Identify the blood parasite species.
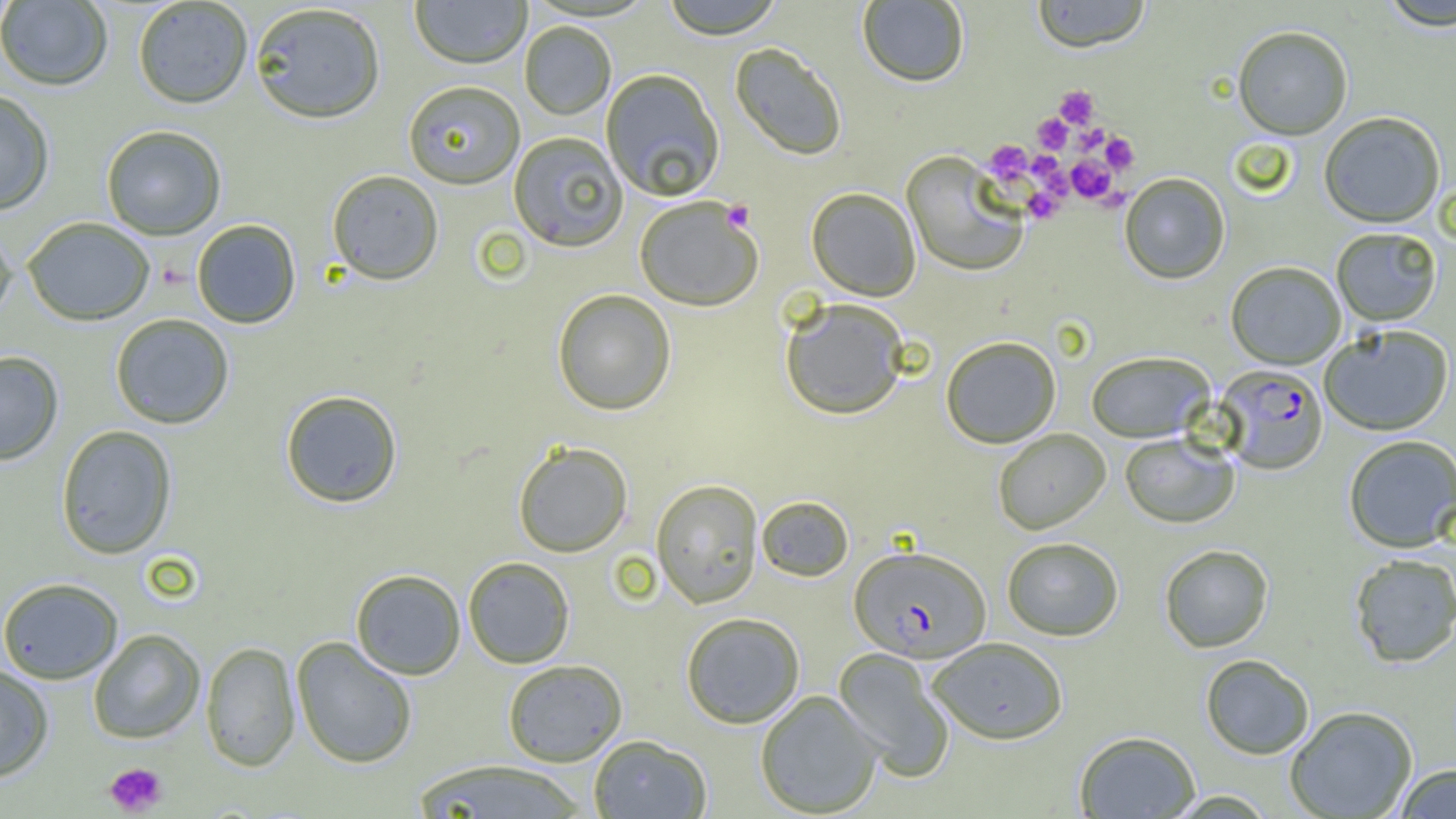

Plasmodium falciparum.

Approximate bounding boxes as named x1/y1/x2/y2 corners in pixels. Platelet locations: (x1=1054, y1=85, x2=1100, y2=128), (x1=1033, y1=113, x2=1071, y2=153), (x1=1074, y1=123, x2=1108, y2=155), (x1=1101, y1=131, x2=1138, y2=174), (x1=984, y1=140, x2=1032, y2=183), (x1=1030, y1=151, x2=1065, y2=184), (x1=1067, y1=155, x2=1114, y2=203), (x1=1024, y1=186, x2=1066, y2=223), (x1=721, y1=199, x2=756, y2=232), (x1=104, y1=762, x2=168, y2=816). Uninfected red blood cell locations: (x1=410, y1=0, x2=531, y2=69), (x1=660, y1=0, x2=785, y2=39), (x1=1031, y1=0, x2=1151, y2=52), (x1=0, y1=1, x2=113, y2=91), (x1=132, y1=1, x2=254, y2=109), (x1=857, y1=1, x2=970, y2=88), (x1=1378, y1=1, x2=1456, y2=32), (x1=249, y1=3, x2=386, y2=124), (x1=519, y1=21, x2=616, y2=120), (x1=1232, y1=27, x2=1353, y2=141), (x1=729, y1=43, x2=847, y2=162), (x1=600, y1=68, x2=725, y2=202), (x1=403, y1=80, x2=525, y2=189), (x1=0, y1=88, x2=55, y2=215), (x1=1319, y1=113, x2=1445, y2=229), (x1=101, y1=124, x2=227, y2=240), (x1=507, y1=131, x2=628, y2=252), (x1=901, y1=152, x2=1030, y2=278), (x1=327, y1=169, x2=444, y2=285), (x1=1119, y1=174, x2=1230, y2=285), (x1=806, y1=187, x2=921, y2=302), (x1=633, y1=196, x2=764, y2=312), (x1=22, y1=217, x2=155, y2=326), (x1=191, y1=219, x2=301, y2=329), (x1=0, y1=222, x2=17, y2=327), (x1=1331, y1=228, x2=1442, y2=327), (x1=1226, y1=262, x2=1346, y2=370), (x1=551, y1=288, x2=677, y2=416), (x1=779, y1=297, x2=911, y2=421), (x1=109, y1=314, x2=235, y2=429), (x1=1320, y1=326, x2=1454, y2=437), (x1=940, y1=336, x2=1062, y2=449), (x1=0, y1=350, x2=64, y2=465), (x1=1086, y1=352, x2=1215, y2=443), (x1=280, y1=389, x2=403, y2=508), (x1=55, y1=425, x2=177, y2=559), (x1=993, y1=429, x2=1111, y2=534), (x1=1120, y1=433, x2=1239, y2=529), (x1=1343, y1=435, x2=1456, y2=553), (x1=512, y1=441, x2=633, y2=557), (x1=651, y1=478, x2=763, y2=608), (x1=756, y1=495, x2=854, y2=582), (x1=1001, y1=537, x2=1124, y2=641), (x1=1159, y1=544, x2=1273, y2=653), (x1=1349, y1=554, x2=1456, y2=668), (x1=463, y1=556, x2=575, y2=668), (x1=350, y1=568, x2=466, y2=680), (x1=0, y1=577, x2=124, y2=684), (x1=680, y1=611, x2=805, y2=729), (x1=88, y1=629, x2=205, y2=744), (x1=291, y1=636, x2=417, y2=769), (x1=927, y1=637, x2=1068, y2=744), (x1=201, y1=641, x2=300, y2=772), (x1=833, y1=648, x2=954, y2=781), (x1=1200, y1=654, x2=1314, y2=760), (x1=502, y1=659, x2=627, y2=766), (x1=0, y1=664, x2=54, y2=782), (x1=755, y1=690, x2=883, y2=817), (x1=1285, y1=706, x2=1418, y2=819), (x1=1074, y1=730, x2=1200, y2=818), (x1=588, y1=734, x2=712, y2=818), (x1=411, y1=760, x2=592, y2=818), (x1=1392, y1=764, x2=1456, y2=818), (x1=1165, y1=790, x2=1278, y2=818). Plasmodium falciparum-infected red blood cell locations: (x1=1215, y1=365, x2=1328, y2=476), (x1=849, y1=546, x2=991, y2=663). One field of a larger specimen. Optical microscopy. Captured at 1000x magnification. Image is 1456×819 pixels. Thin blood film.